Describe the morphology of the erythrocytes.
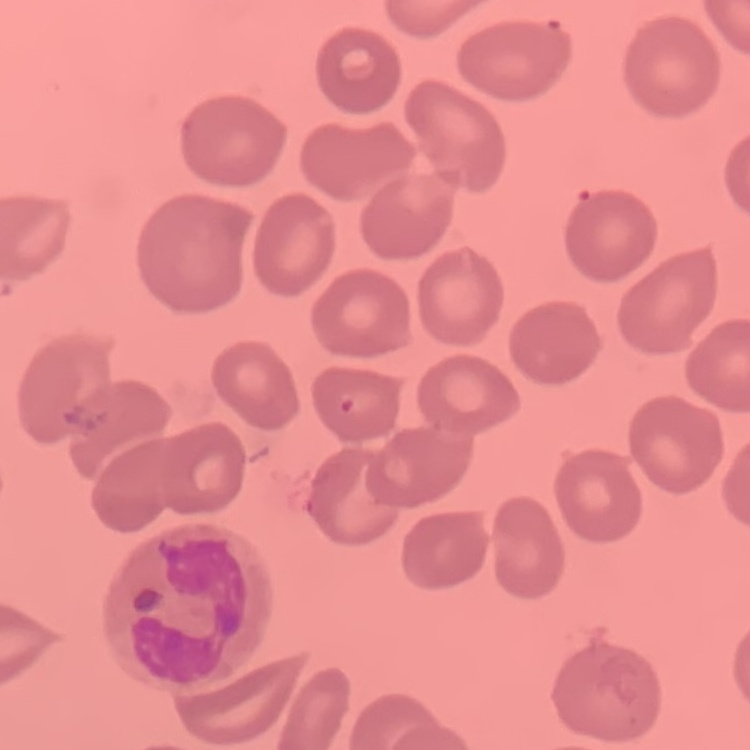
They show no rouleaux formation.

Thin blood film. One tile cut from a larger photomicrograph. Stained with either Field's or Giemsa.